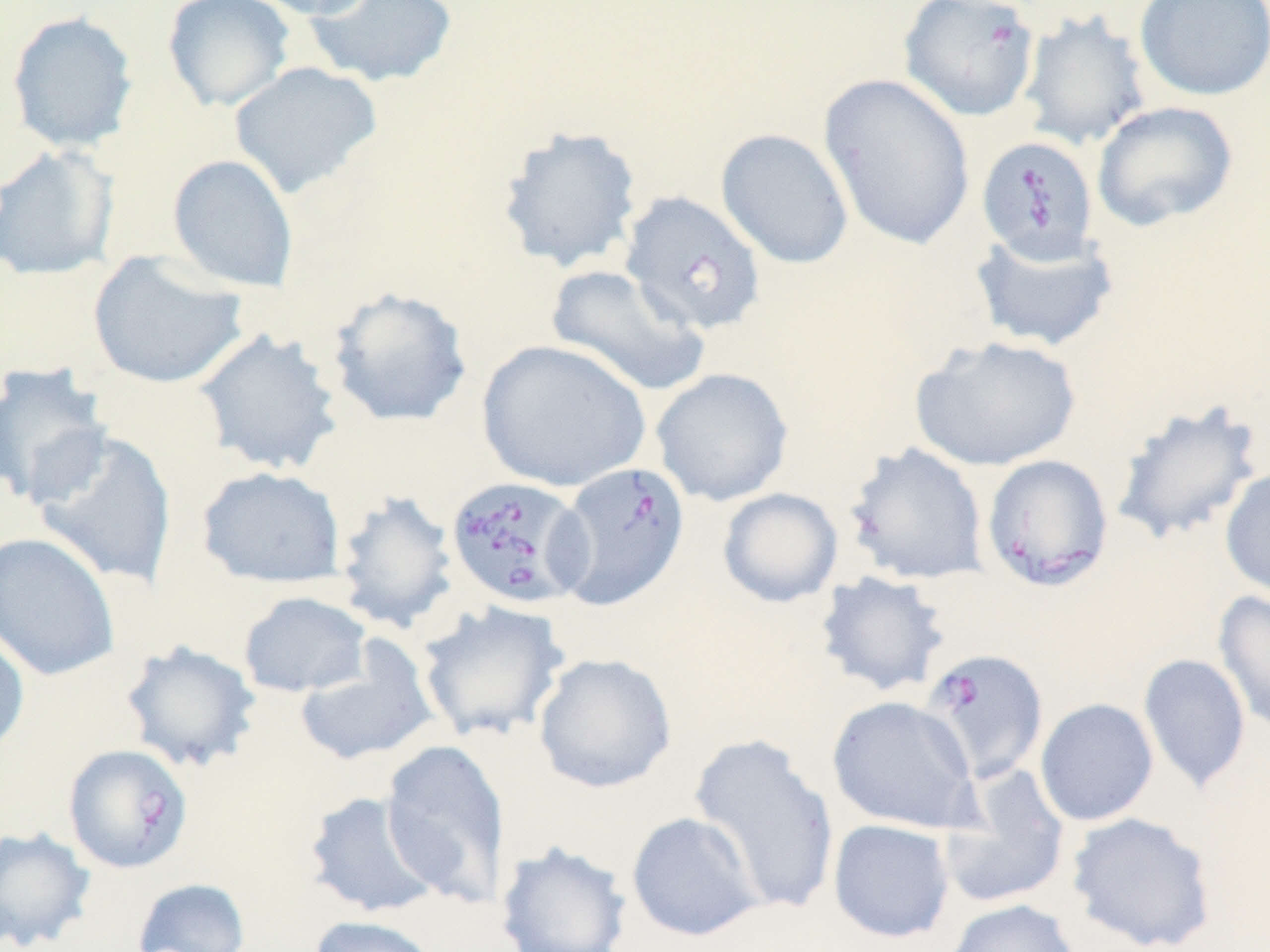

Approximate bounding boxes as (x1, y1, x2, y2) in pixels. Uninfected red blood cell locations: (161, 0, 296, 112), (246, 0, 381, 20), (303, 0, 459, 89), (1133, 0, 1270, 102), (1017, 9, 1153, 152), (6, 10, 139, 153), (228, 61, 384, 200), (817, 74, 976, 252), (1091, 101, 1239, 232), (496, 124, 644, 274), (716, 128, 854, 269), (0, 143, 120, 282), (167, 153, 299, 293), (620, 191, 766, 335), (967, 227, 1120, 353), (86, 251, 248, 389), (544, 264, 712, 398), (324, 285, 474, 428), (191, 328, 345, 477), (909, 335, 1082, 472), (476, 338, 650, 493), (0, 361, 113, 509), (650, 367, 794, 507), (1108, 397, 1268, 547), (31, 429, 179, 591), (843, 441, 989, 585), (196, 465, 347, 589), (1219, 466, 1270, 600), (717, 487, 843, 608), (332, 489, 460, 635), (0, 531, 121, 682), (814, 571, 953, 698), (1213, 589, 1270, 737), (238, 591, 372, 698), (416, 599, 572, 744), (0, 629, 31, 758), (119, 639, 263, 774), (294, 639, 440, 767), (532, 652, 678, 794), (1137, 652, 1251, 793), (826, 694, 980, 834), (1035, 698, 1158, 826), (687, 733, 841, 915), (380, 738, 511, 906), (938, 764, 1071, 911), (301, 789, 444, 919), (626, 811, 764, 942), (1065, 811, 1218, 952), (827, 818, 955, 943), (0, 826, 97, 951), (494, 840, 632, 952), (132, 877, 250, 952), (943, 899, 1081, 952), (306, 914, 441, 952). Babesia divergens-infected red blood cell locations: (898, 0, 1041, 122), (976, 135, 1100, 265), (980, 454, 1114, 591), (550, 461, 690, 610), (444, 475, 590, 609), (919, 648, 1050, 785), (67, 745, 197, 874). Slide-level diagnosis: Babesia divergens. Light microscopy. One field of a larger specimen. Image is 1270×952 pixels. Thin blood film. May-Grünwald-Giemsa-stained preparation. Captured at 1000x magnification.